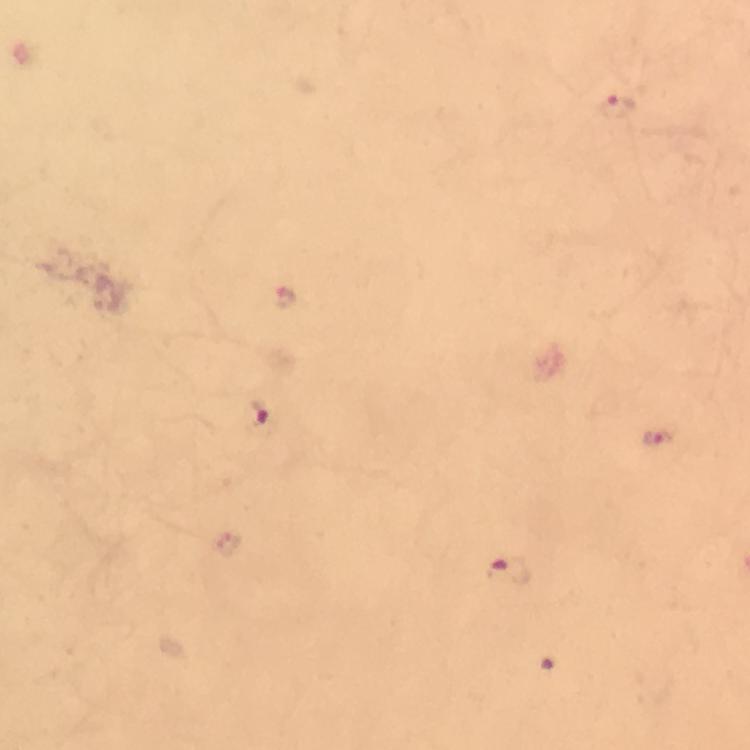

Approximate centers as (x, y) in pixels.
Summary:
  - Malaria parasite locations: (616, 109), (284, 298), (254, 416), (657, 437), (508, 572)
  - Image size: 750×750 pixels
  - Cropped from: a single field of view
  - Immersion oil: used
  - Preparation: thick blood smear
  - Context: from a diagnostic examination for malaria
  - Capture: smartphone photograph through a microscope
  - Stain: Giemsa
  - Magnification: 100x